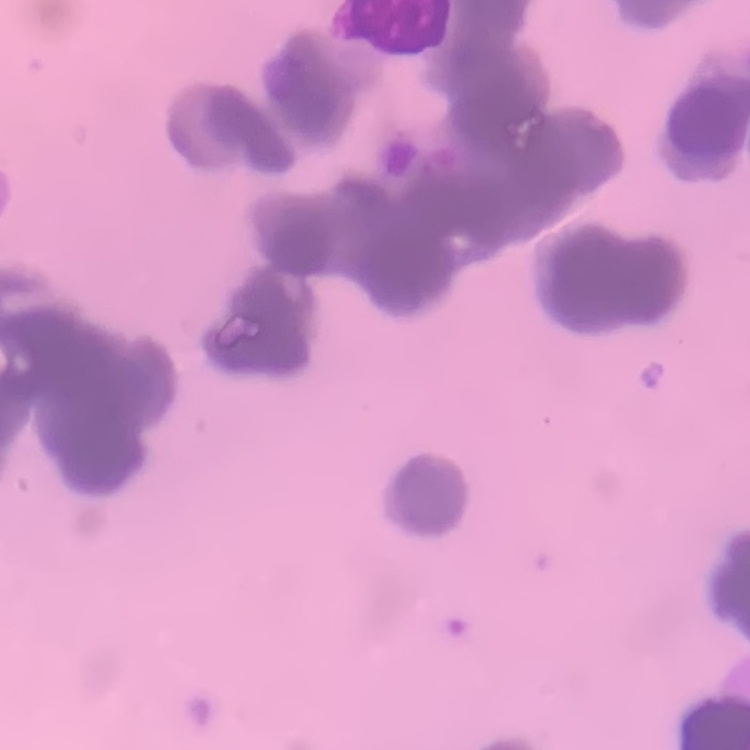
erythrocyte morphology = rouleaux formation
stain = Field's or Giemsa
preparation = thin peripheral smear
image type = square crop of a larger photomicrograph